Assess this cell for malaria.
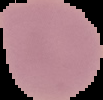

Uninfected.

image type = segmented cell region on a black background
image size = 103×100 pixels
preparation = thin blood film